Locate Plasmodium falciparum parasites and identify their life-cycle stages.
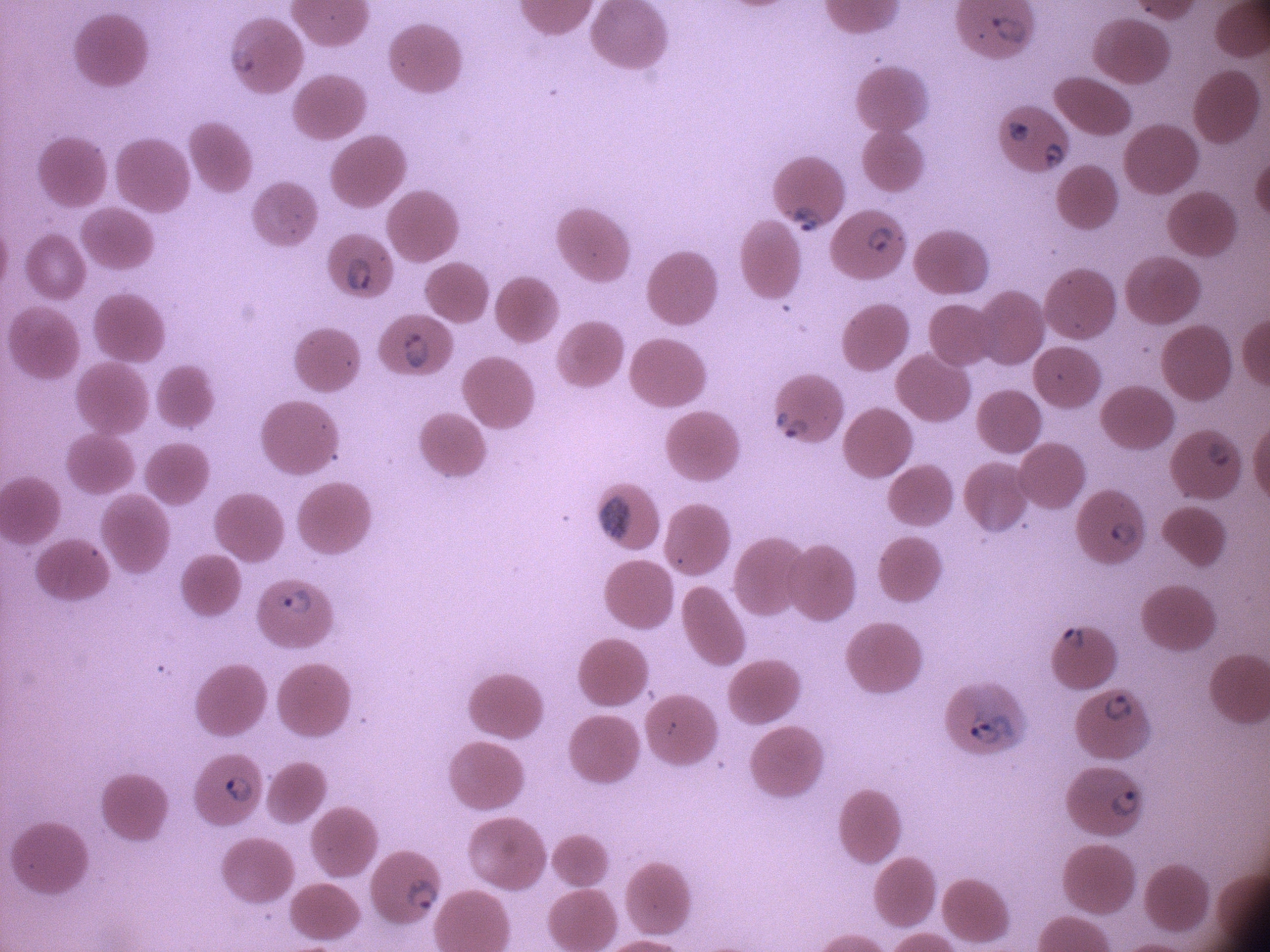

Approximate bounding boxes as named x1/y1/x2/y2 corners in pixels, from the source annotation, which is not necessarily exhaustive.
Ring forms: (x1=988, y1=9, x2=1032, y2=48), (x1=1005, y1=118, x2=1035, y2=146), (x1=1039, y1=137, x2=1068, y2=173), (x1=776, y1=199, x2=829, y2=241), (x1=859, y1=221, x2=903, y2=259), (x1=339, y1=247, x2=377, y2=296), (x1=395, y1=329, x2=432, y2=373), (x1=770, y1=409, x2=811, y2=445), (x1=1204, y1=432, x2=1240, y2=471), (x1=1106, y1=515, x2=1143, y2=549), (x1=272, y1=584, x2=318, y2=619), (x1=1056, y1=624, x2=1093, y2=656), (x1=1098, y1=689, x2=1138, y2=726), (x1=962, y1=708, x2=1019, y2=745), (x1=219, y1=772, x2=259, y2=806), (x1=1107, y1=783, x2=1146, y2=822), (x1=402, y1=875, x2=441, y2=916).

Summary:
  - Stain: Giemsa
  - Microscope: Leica DM2000 with built-in camera
  - Magnification: 100x
  - Species: Plasmodium falciparum
  - Preparation: thin blood film
  - Field of view: one from this slide
  - Image size: 1270×952 pixels